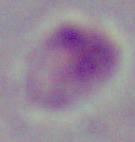

1000x magnification. A Leishmania parasite is seen. Photomicrograph.